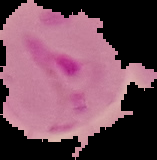
Result: Plasmodium parasites detected. Cell region segmented out of the field of view; the surrounding area is masked to black. Image is 157×160 pixels. From a thin blood film.